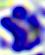 400x magnification. A white blood cell is shown. Photomicrograph.